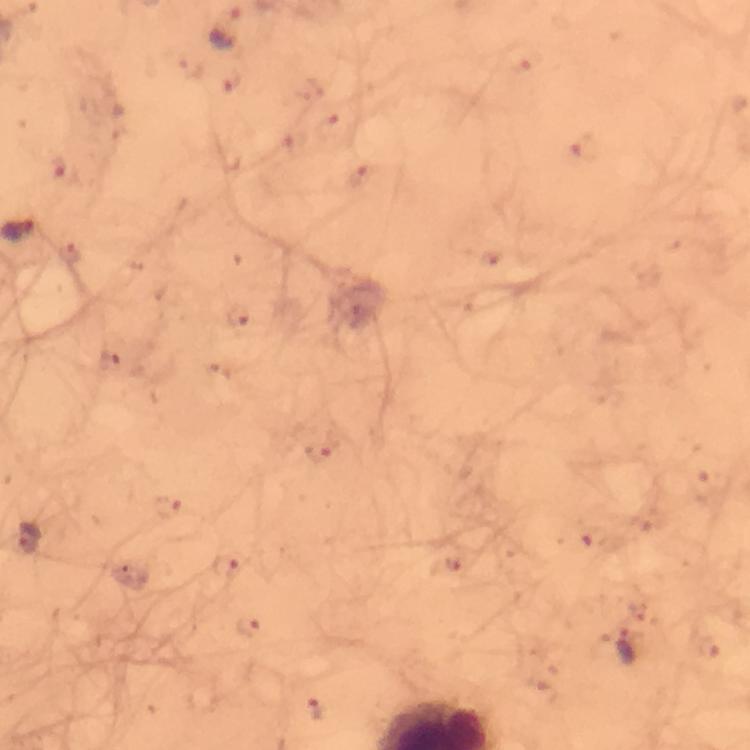
Approximate centers as {x, y} in pixels.
Summary:
  - Plasmodium parasite locations: {224, 28}, {521, 58}, {232, 82}, {332, 125}, {583, 149}, {64, 169}, {359, 177}, {239, 318}, {110, 364}, {318, 453}, {165, 505}, {28, 539}, {596, 540}, {451, 563}, {225, 566}, {248, 627}, {625, 646}, {712, 647}, {316, 706}
  - Immersion oil: used
  - Capture: smartphone camera through the microscope
  - Context: from a malaria diagnostic workup
  - Preparation: thick smear
  - Stain: Giemsa
  - Cropped from: one field of view
  - Magnification: 100x
  - Image size: 750×750 pixels